Describe the morphology of the red blood cells.
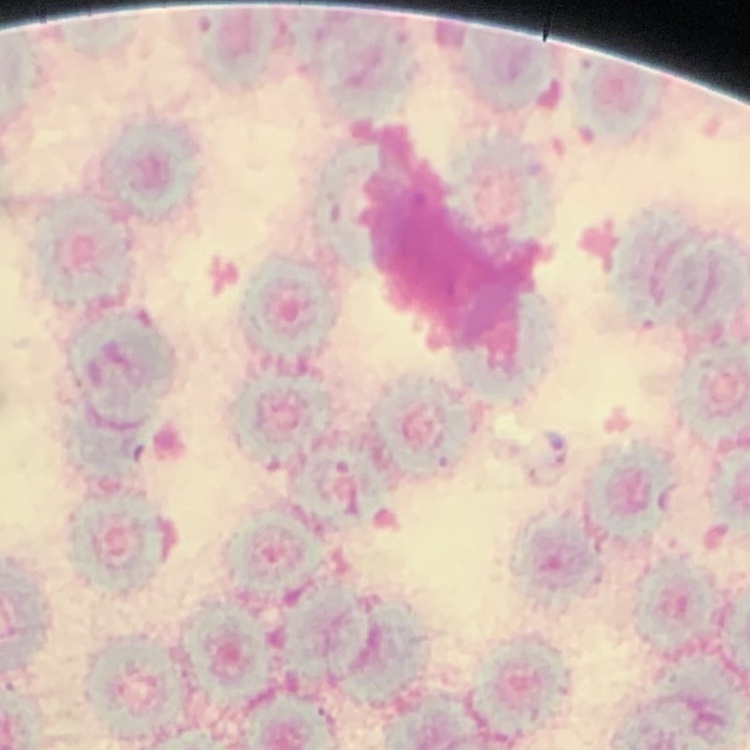

They show rouleaux formation.

preparation = thin blood smear
image type = one tile cut from a larger photomicrograph
stain = Field's or Giemsa